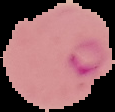

preparation = thin blood film
image size = 115×112 pixels
image type = segmented cell region with the area outside set to black
malaria status = parasitized